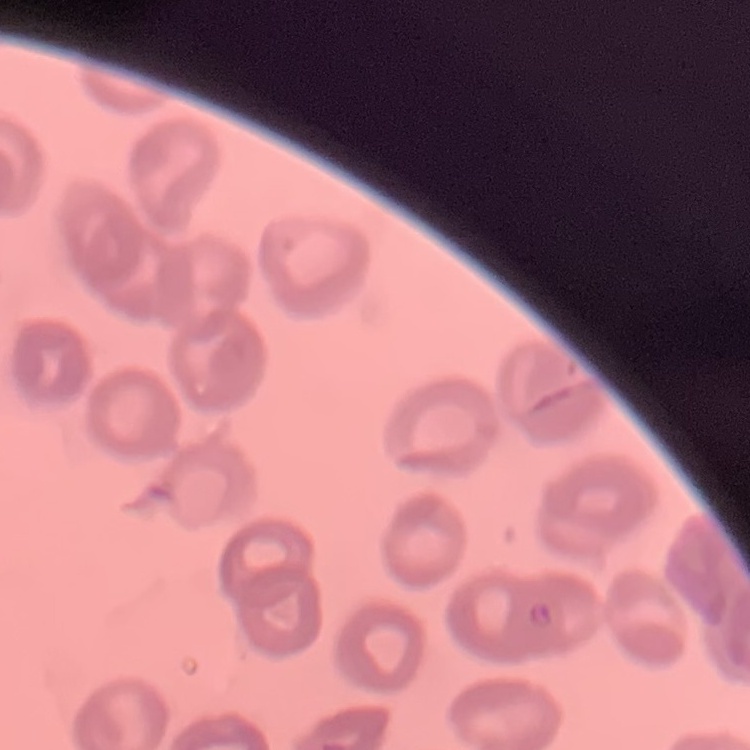

The red blood cells show no rouleaux formation. Field's or Giemsa stain. Thin blood film. One tile cut from a larger photomicrograph.